Outline each Plasmodium malariae-infected red blood cell.
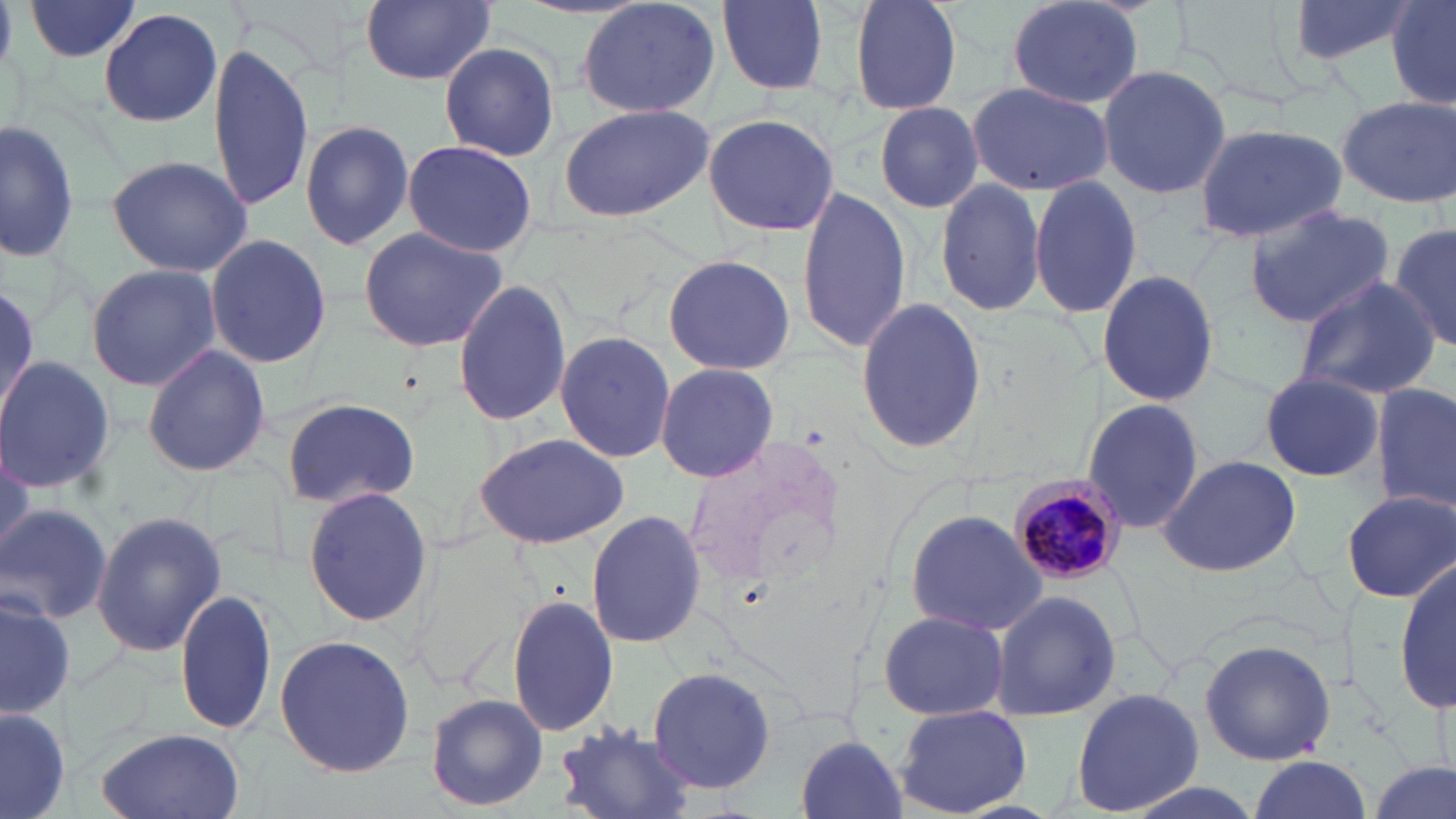
Approximate bounding boxes as (x1, y1, x2, y2) in pixels.
Plasmodium malariae-infected red blood cells: (1010, 474, 1130, 584).

slide-level diagnosis = Plasmodium malariae
stain = May-Grünwald-Giemsa
image size = 1456×819 pixels
uninfected red blood cell locations = approximate bounding boxes as (x1, y1, x2, y2) in pixels: (21, 0, 145, 63), (359, 0, 496, 85), (712, 0, 834, 96), (846, 0, 965, 115), (1002, 0, 1149, 109), (1282, 0, 1418, 70), (1385, 0, 1456, 110), (575, 1, 723, 120), (99, 8, 224, 129), (438, 41, 560, 162), (207, 42, 316, 210), (1097, 63, 1231, 201), (967, 81, 1113, 195), (1337, 96, 1455, 206), (557, 102, 716, 223), (873, 103, 985, 213), (703, 114, 840, 238), (0, 115, 76, 259), (299, 120, 414, 250), (1195, 121, 1348, 243), (402, 140, 537, 257), (106, 154, 254, 278), (934, 176, 1047, 317), (1027, 176, 1144, 318), (796, 184, 911, 355), (1241, 205, 1394, 327), (1388, 218, 1455, 358), (355, 226, 511, 355), (205, 234, 333, 368), (662, 253, 797, 376), (85, 264, 223, 392), (1097, 268, 1220, 408), (1293, 275, 1440, 401), (453, 276, 573, 428), (853, 294, 987, 456), (553, 332, 675, 464), (142, 343, 270, 477), (0, 355, 115, 494), (654, 362, 778, 484), (1257, 369, 1384, 483), (1371, 383, 1455, 511), (279, 396, 422, 511), (1081, 398, 1205, 538), (474, 432, 629, 550), (1156, 453, 1305, 578), (303, 486, 433, 627), (1346, 490, 1455, 603), (0, 501, 113, 625), (903, 507, 1048, 637), (586, 511, 706, 649), (90, 512, 227, 657), (1395, 555, 1454, 720), (175, 588, 279, 736), (990, 589, 1120, 721), (0, 591, 74, 721), (507, 595, 618, 739), (874, 610, 1013, 721), (272, 634, 414, 778), (1199, 639, 1339, 765), (651, 663, 777, 796), (1071, 688, 1203, 813), (426, 693, 549, 811), (895, 705, 1032, 817), (0, 706, 72, 818), (549, 719, 700, 819), (93, 727, 246, 819), (792, 734, 911, 819), (1244, 756, 1376, 819), (1365, 759, 1453, 819)
modality = optical microscopy
magnification = 1000x
preparation = thin blood film
field of view = one of a larger specimen